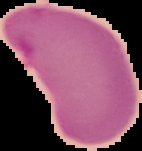 Image is 142×151 pixels. The area outside the segmented cell region is set to black. Result: no Plasmodium parasites detected. From a thin blood film.